Report the malaria status of this cell.
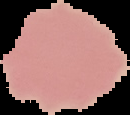

Uninfected.

Image is 130×115 pixels. Segmented cell region on a black background. From a thin blood smear.